Identify the parasite.
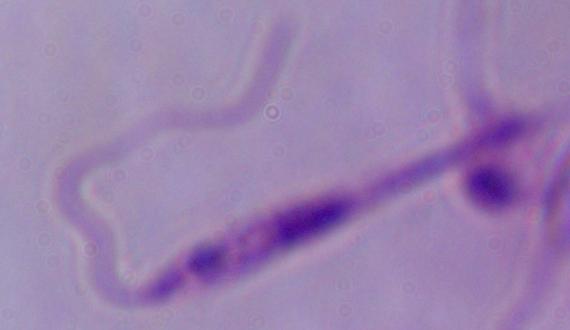

Leishmania.

Summary:
  - Modality: photomicrograph
  - Magnification: 1000x